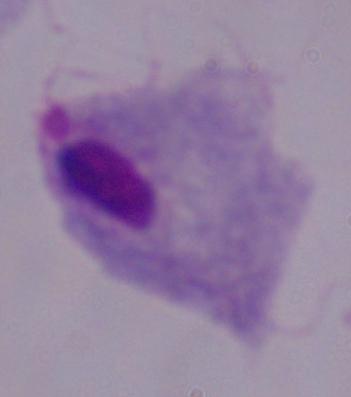

Summary:
  - Modality: micrograph
  - Magnification: 1000x
  - Identification: trichomonad